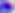
Micrograph. Toxoplasma gondii is seen. 400x magnification.